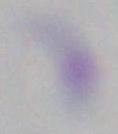 1000x magnification. Photomicrograph. Toxoplasma gondii is seen.